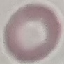

Summary:
  - Result: no malaria parasites seen
  - Stain: Giemsa
  - Preparation: thin blood smear
  - Image type: cell patch, automatically extracted from a larger field of view and resized to 64 × 64 pixels
  - Capture: smartphone camera at the microscope eyepiece